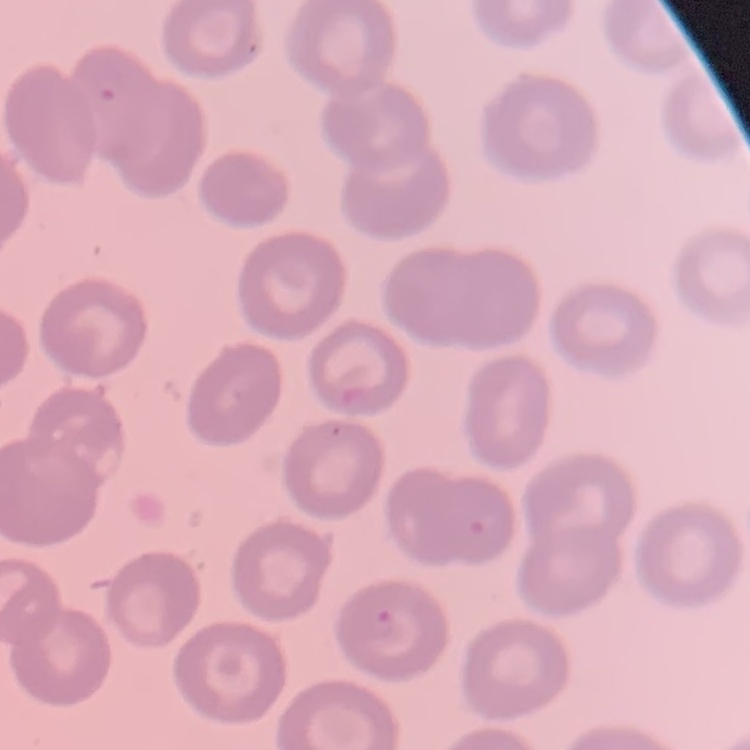
Summary:
  - Erythrocyte morphology: no rouleaux formation
  - Stain: Field's or Giemsa
  - Preparation: thin blood smear
  - Image type: square crop of a larger photomicrograph